Identify the parasite.
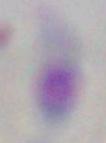

Toxoplasma gondii.

{
  "magnification": "1000x",
  "modality": "photomicrograph"
}